Classify this cell by malaria status.
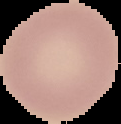
It is uninfected.

{
  "preparation": "thin blood film",
  "image_size": "121×124 pixels",
  "image_type": "segmented cell region with the area outside set to black"
}